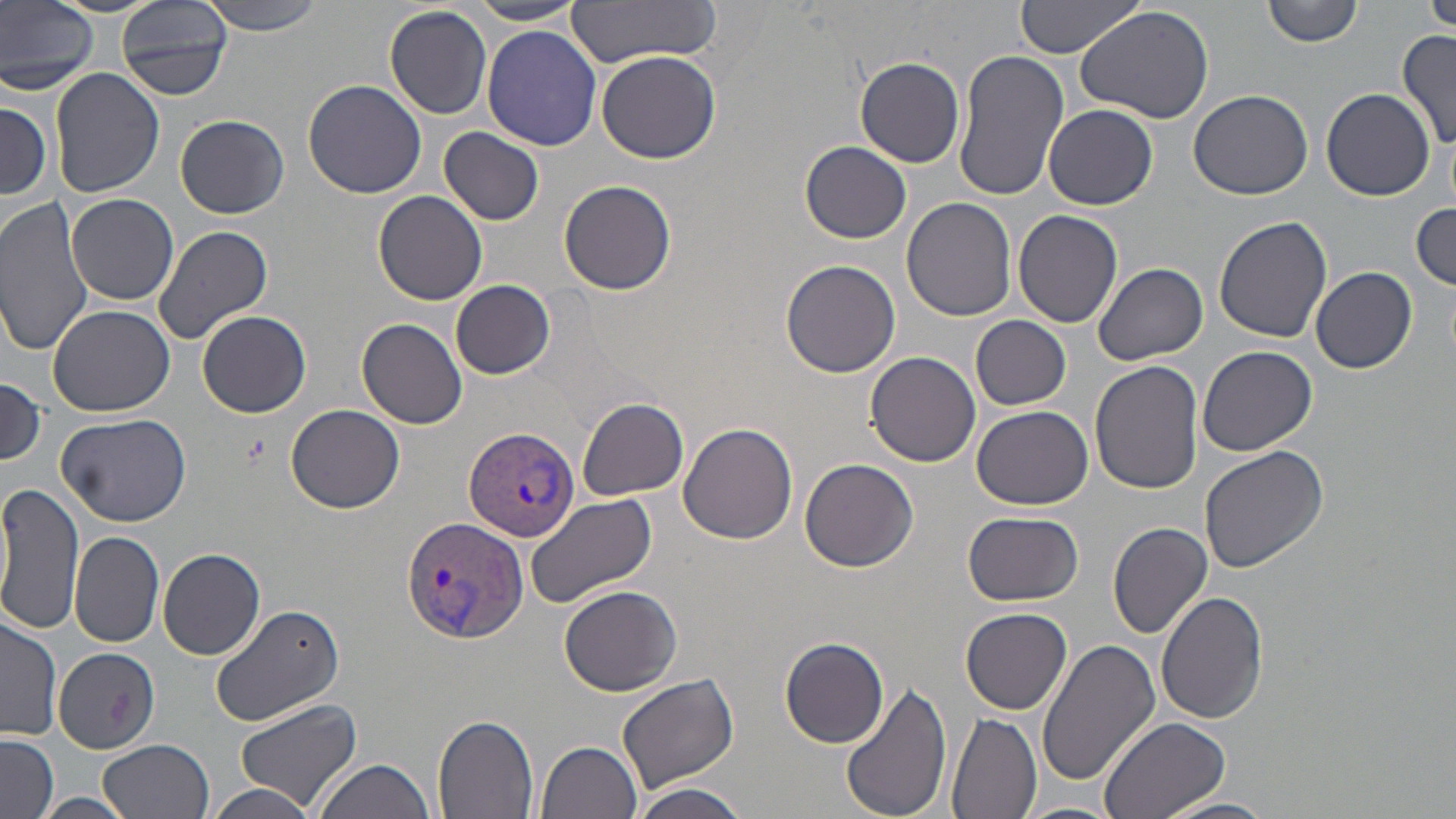

Summary:
  - Coordinate format: approximate bounding boxes as [x1, y1, x2, y2] in pixels
  - Uninfected red blood cell locations: [0, 0, 99, 94], [46, 0, 165, 17], [117, 0, 231, 101], [200, 0, 327, 37], [563, 0, 726, 66], [1014, 0, 1150, 57], [1262, 0, 1365, 47], [1424, 0, 1456, 38], [468, 1, 585, 25], [384, 4, 493, 120], [1075, 6, 1214, 123], [480, 26, 602, 150], [1398, 30, 1455, 155], [952, 49, 1070, 203], [595, 50, 723, 165], [856, 57, 967, 168], [50, 66, 165, 198], [303, 80, 427, 200], [1187, 88, 1313, 202], [1321, 88, 1434, 200], [0, 96, 54, 201], [1044, 105, 1158, 211], [175, 114, 288, 217], [439, 127, 545, 226], [800, 141, 911, 243], [558, 179, 678, 295], [8, 185, 162, 392], [375, 190, 487, 307], [66, 193, 179, 306], [0, 195, 99, 357], [902, 196, 1017, 320], [1411, 199, 1455, 290], [1013, 211, 1123, 328], [1214, 214, 1333, 343], [152, 224, 274, 345], [780, 259, 902, 377], [1094, 262, 1209, 366], [1311, 267, 1417, 373], [451, 280, 555, 379], [49, 305, 175, 416], [196, 310, 311, 419], [971, 315, 1071, 410], [357, 318, 467, 430], [1198, 347, 1318, 458], [865, 352, 981, 467], [1090, 360, 1204, 495], [0, 381, 46, 466], [575, 398, 689, 500], [971, 403, 1092, 510], [286, 404, 405, 512], [57, 412, 191, 527], [678, 422, 798, 545], [1199, 446, 1332, 574], [800, 458, 919, 572], [0, 482, 84, 637], [524, 492, 658, 609], [962, 512, 1084, 606], [1108, 522, 1212, 639], [70, 531, 165, 647], [157, 547, 265, 660], [558, 585, 683, 697], [1156, 590, 1268, 723], [209, 602, 345, 726], [961, 607, 1073, 714], [0, 613, 61, 740], [1037, 635, 1160, 788], [779, 637, 889, 749], [53, 647, 161, 753], [618, 673, 739, 793], [840, 679, 953, 819], [233, 698, 364, 817], [946, 712, 1040, 819], [432, 713, 538, 819], [1098, 716, 1230, 819], [0, 734, 59, 819], [99, 739, 214, 819], [535, 739, 644, 819], [316, 758, 437, 819], [634, 783, 751, 819], [207, 784, 316, 819], [35, 792, 136, 819], [1157, 795, 1279, 819], [1013, 801, 1127, 819]
  - Plasmodium vivax-infected red blood cell locations: [462, 426, 578, 543], [401, 515, 529, 645]
  - Slide-level diagnosis: Plasmodium vivax
  - Magnification: 1000x
  - Image size: 1456×819 pixels
  - Field of view: single
  - Preparation: thin blood smear
  - Modality: optical microscopy
  - Stain: May-Grünwald-Giemsa